Comment on the morphology of the red blood cells.
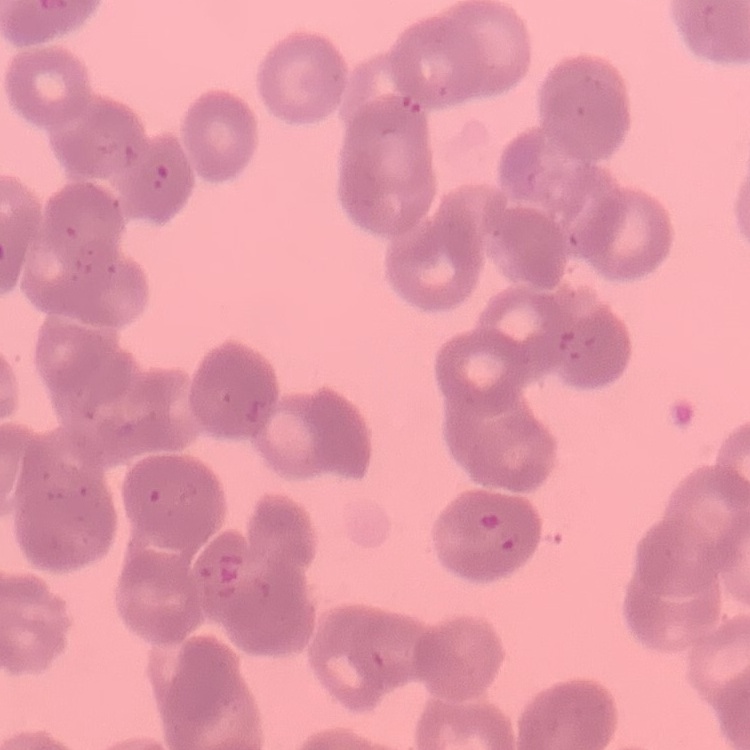
Rouleaux formation.

Thin blood smear. One tile cut from a larger photomicrograph. Stained with either Field's or Giemsa.